Identify the parasite.
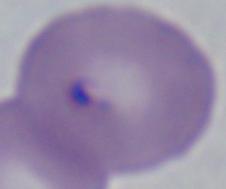
This is Babesia.

modality = photomicrograph
magnification = 1000x